Comment on the morphology of the red blood cells.
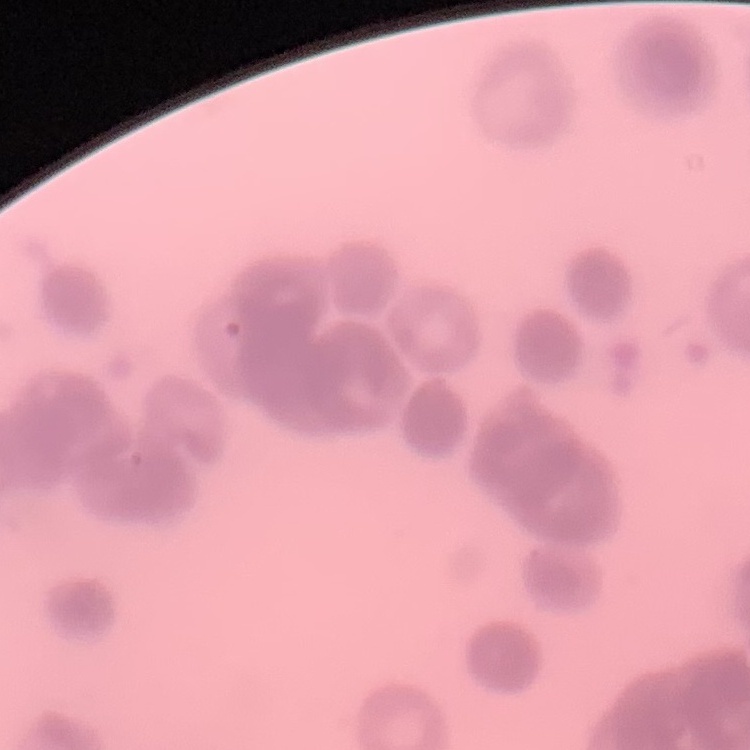

They show rouleaux formation.

Summary:
  - Preparation: thin blood film
  - Stain: Field's or Giemsa
  - Image type: one tile cut from a larger photomicrograph